Assess this cell for malaria.
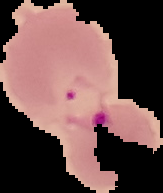
It is parasitized.

Summary:
  - Image type: cell region segmented out of the field of view; surrounding area masked to black
  - Preparation: thin blood film
  - Image size: 163×193 pixels